Assess the morphology of the erythrocytes.
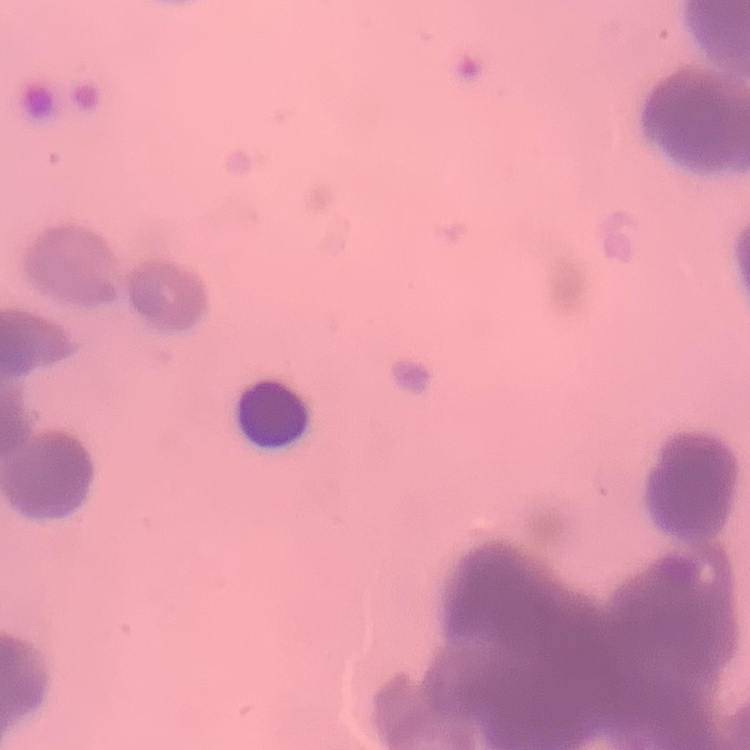

They show rouleaux formation.

Summary:
  - Image type: one tile cut from a larger photomicrograph
  - Preparation: thin blood smear
  - Stain: Field's or Giemsa